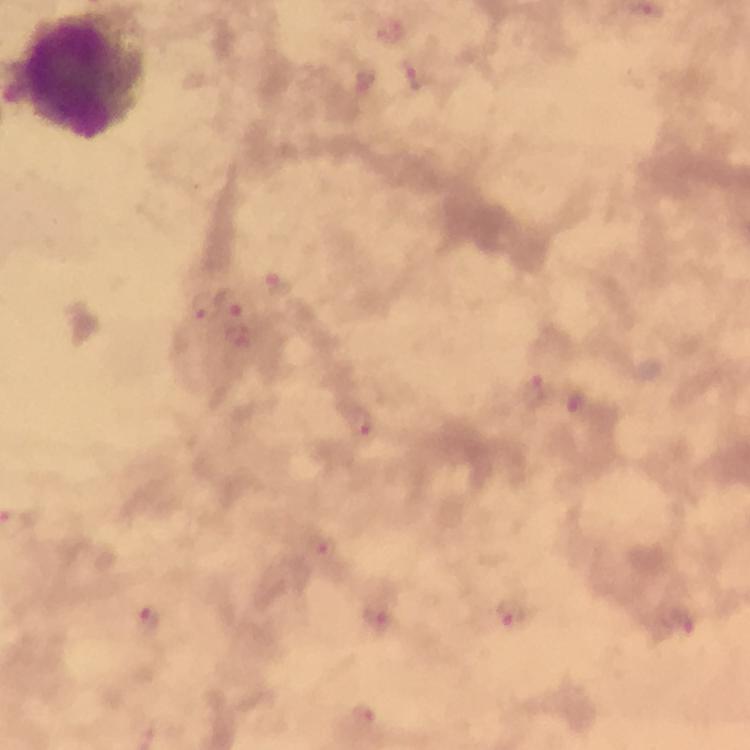
Approximate object centers, in pixels from the top-left corner.
Summary:
  - Malaria parasite locations: (x=389, y=29), (x=410, y=77), (x=364, y=83), (x=276, y=286), (x=230, y=302), (x=202, y=306), (x=533, y=391), (x=574, y=401), (x=362, y=421), (x=321, y=547), (x=511, y=612), (x=148, y=618), (x=377, y=618), (x=682, y=621), (x=361, y=715)
  - Leukocyte locations: (x=83, y=78)
  - Context: from a diagnostic examination for malaria
  - Stain: Giemsa
  - Immersion oil: used
  - Magnification: 100x
  - Capture: smartphone mounted on the microscope
  - Cropped from: a single field of view
  - Image size: 750×750 pixels
  - Preparation: thick blood smear